Report the malaria status of this cell.
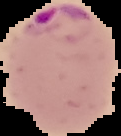

Parasitized.

Summary:
  - Image type: segmented cell region on a black background
  - Preparation: thin blood smear
  - Image size: 121×136 pixels